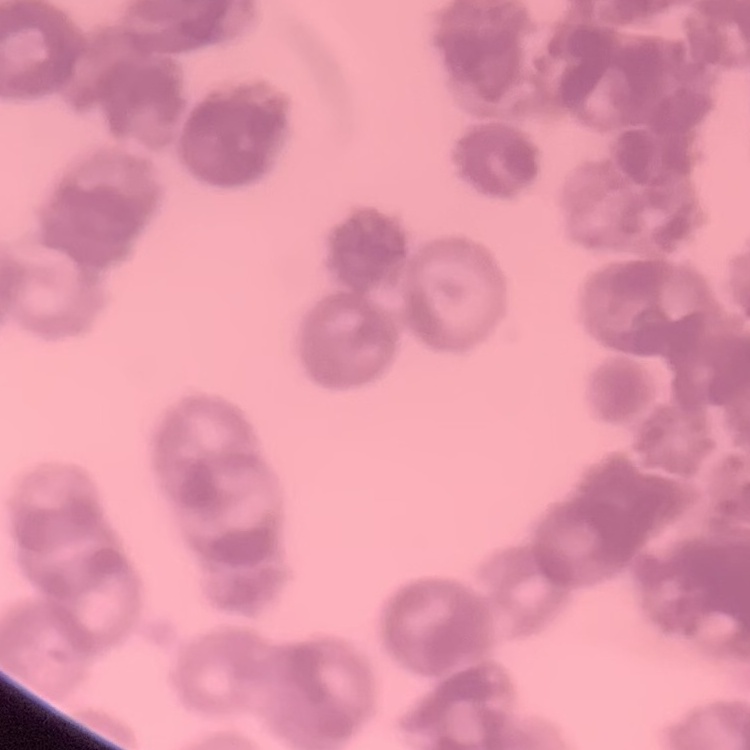

Summary:
  - Red blood cell morphology: rouleaux formation
  - Stain: Field's or Giemsa
  - Image type: square crop of a larger photomicrograph
  - Preparation: thin blood film